State which parasite is depicted.
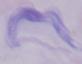
A trypanosome.

1000x magnification. Micrograph.